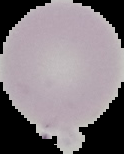

Summary:
  - Preparation: thin blood film
  - Malaria status: uninfected
  - Image type: segmented cell region with the area outside set to black
  - Image size: 124×154 pixels